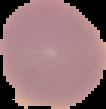 Image is 106×109 pixels. Segmented cell region on a black background. Result: negative for malaria parasites. From a thin blood smear.